Name the parasite shown.
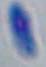
This is Toxoplasma gondii.

Summary:
  - Magnification: 1000x
  - Modality: photomicrograph